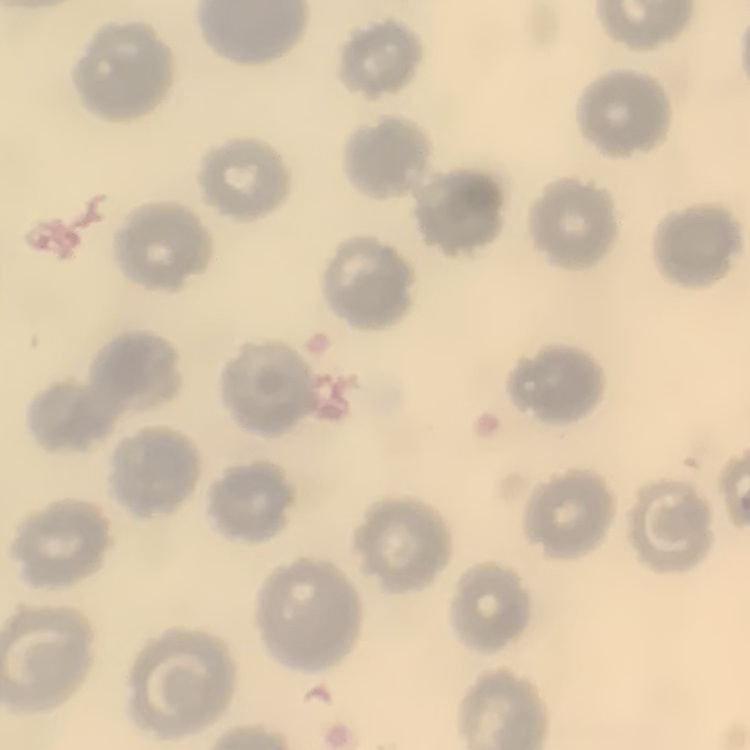
{
  "erythrocyte_morphology": "no rouleaux formation",
  "image_type": "square crop of a larger photomicrograph",
  "preparation": "thin blood smear",
  "stain": "Field's or Giemsa"
}